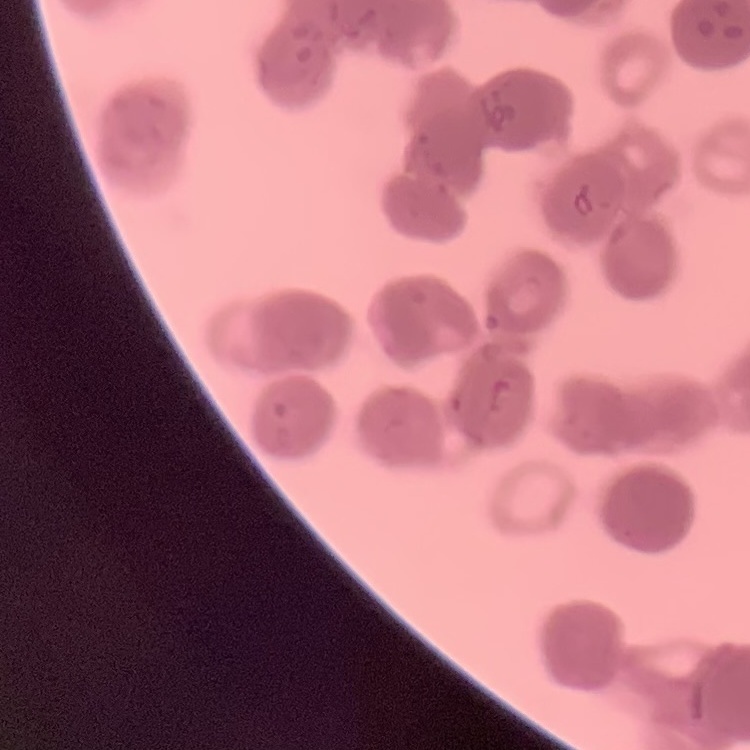
erythrocyte morphology = rouleaux formation
image type = square crop of a larger photomicrograph
stain = Field's or Giemsa
preparation = thin peripheral smear